Locate and identify every blood parasite.
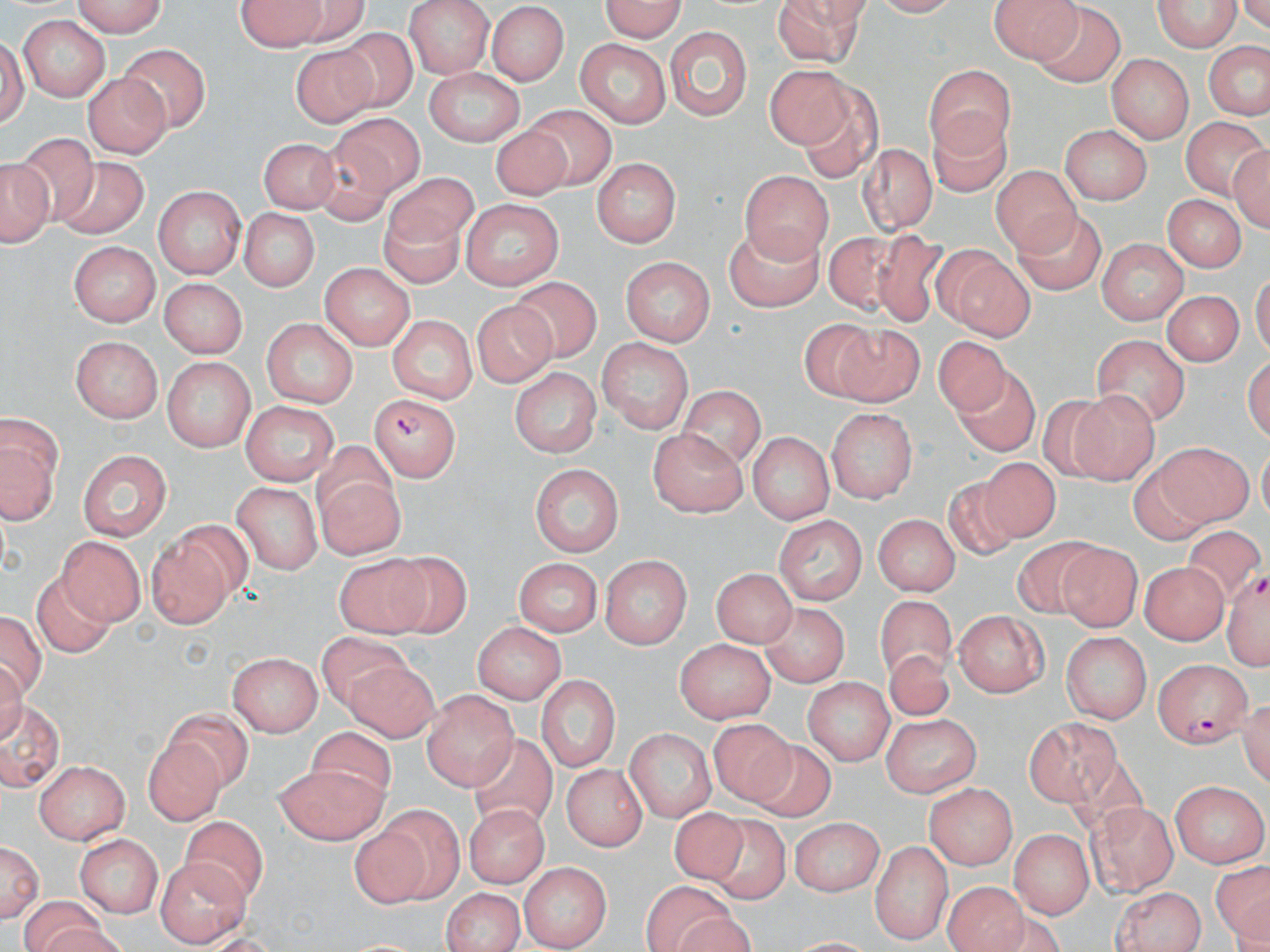

Approximate bounding boxes as (x1,y1)-(x2,y2) corner pairs in pixels.
Plasmodium falciparum-infected red blood cells: (371,390)-(466,481), (1229,567)-(1270,673), (1155,656)-(1250,745).
No Plasmodium ovale, Plasmodium malariae, Plasmodium vivax, Babesia divergens, or Trypanosoma brucei observed.

Uninfected red blood cell locations: (66,0)-(167,35), (403,0)-(495,76), (593,0)-(688,40), (994,0)-(1080,63), (1152,0)-(1241,54), (778,1)-(869,67), (237,3)-(352,49), (489,5)-(570,84), (1038,7)-(1127,92), (16,16)-(110,102), (667,20)-(751,123), (333,29)-(419,112), (2,35)-(32,137), (1204,39)-(1269,120), (122,40)-(208,133), (574,40)-(672,126), (290,42)-(384,130), (1107,55)-(1192,144), (927,63)-(1018,153), (768,64)-(846,146), (425,68)-(525,147), (82,72)-(170,158), (800,86)-(881,188), (521,102)-(613,190), (928,108)-(1009,199), (330,116)-(423,195), (1175,119)-(1265,204), (1058,124)-(1149,204), (491,126)-(571,203), (260,133)-(337,217), (13,136)-(101,230), (311,136)-(394,227), (1229,140)-(1270,232), (857,141)-(938,233), (1,153)-(57,248), (592,157)-(682,249), (52,158)-(153,239), (991,162)-(1083,251), (740,168)-(834,257), (380,176)-(483,251), (154,185)-(244,280), (1163,194)-(1242,273), (456,198)-(565,288), (236,208)-(322,294), (375,210)-(469,290), (1016,210)-(1107,295), (720,221)-(826,315), (821,230)-(904,312), (875,230)-(949,328), (1100,237)-(1190,324), (71,239)-(161,325), (933,245)-(1036,342), (619,257)-(717,344), (318,264)-(416,349), (161,275)-(247,358), (506,279)-(600,364), (1164,292)-(1241,372), (473,304)-(558,393), (386,315)-(475,405), (797,315)-(876,407), (264,317)-(357,409), (836,317)-(923,403), (72,335)-(164,420), (1092,335)-(1184,425), (600,337)-(694,435), (933,339)-(1012,416), (157,357)-(253,452), (512,365)-(600,454), (952,368)-(1038,453), (682,383)-(765,469), (1068,389)-(1156,483), (1041,398)-(1115,482), (241,399)-(340,483), (829,407)-(920,504), (2,418)-(58,526), (653,428)-(750,517), (748,431)-(832,522), (313,443)-(395,518), (75,446)-(177,539), (1153,448)-(1255,525), (972,453)-(1069,538), (529,461)-(626,554), (1124,462)-(1208,547), (313,474)-(407,558), (938,477)-(1015,567), (231,478)-(324,570), (873,511)-(960,600), (773,512)-(869,605), (146,516)-(249,630), (1185,524)-(1259,587), (57,534)-(142,624), (1010,536)-(1099,615), (1058,544)-(1137,630), (334,552)-(435,633), (600,555)-(690,649), (382,556)-(468,639), (513,558)-(600,636), (1139,560)-(1230,642), (708,563)-(799,646), (34,570)-(115,658), (877,596)-(956,681), (761,604)-(847,690), (1,609)-(44,705), (956,610)-(1050,699), (474,621)-(566,705), (1062,631)-(1151,725), (313,634)-(412,712), (675,637)-(775,726), (226,649)-(324,738), (883,649)-(955,726), (345,660)-(438,739), (536,673)-(620,774), (802,676)-(892,763), (422,687)-(517,790), (2,696)-(61,789), (166,708)-(255,790), (879,716)-(985,798), (713,719)-(796,809), (1025,719)-(1118,806), (316,728)-(394,805), (625,728)-(716,823), (475,731)-(558,838), (140,739)-(232,826), (749,741)-(830,823), (32,760)-(130,840), (561,760)-(648,849), (274,763)-(386,844), (1172,779)-(1268,868), (925,782)-(1020,866), (1089,799)-(1178,896), (377,802)-(466,904), (670,802)-(747,888), (463,803)-(549,886), (181,811)-(269,910), (706,811)-(786,908), (789,814)-(885,895), (357,826)-(431,914), (1009,828)-(1090,918), (73,832)-(162,916), (869,835)-(953,941), (1,837)-(44,924), (159,857)-(248,949), (517,859)-(608,948), (1210,864)-(1269,950), (940,882)-(1029,952), (640,883)-(734,952), (1113,885)-(1206,951), (438,887)-(527,950), (21,895)-(105,952). Slide-level diagnosis: Plasmodium falciparum. Captured at 1000x magnification. Light microscopy. Single field of view. Thin blood film. Image is 1270×952 pixels. May-Grünwald-Giemsa-stained preparation.